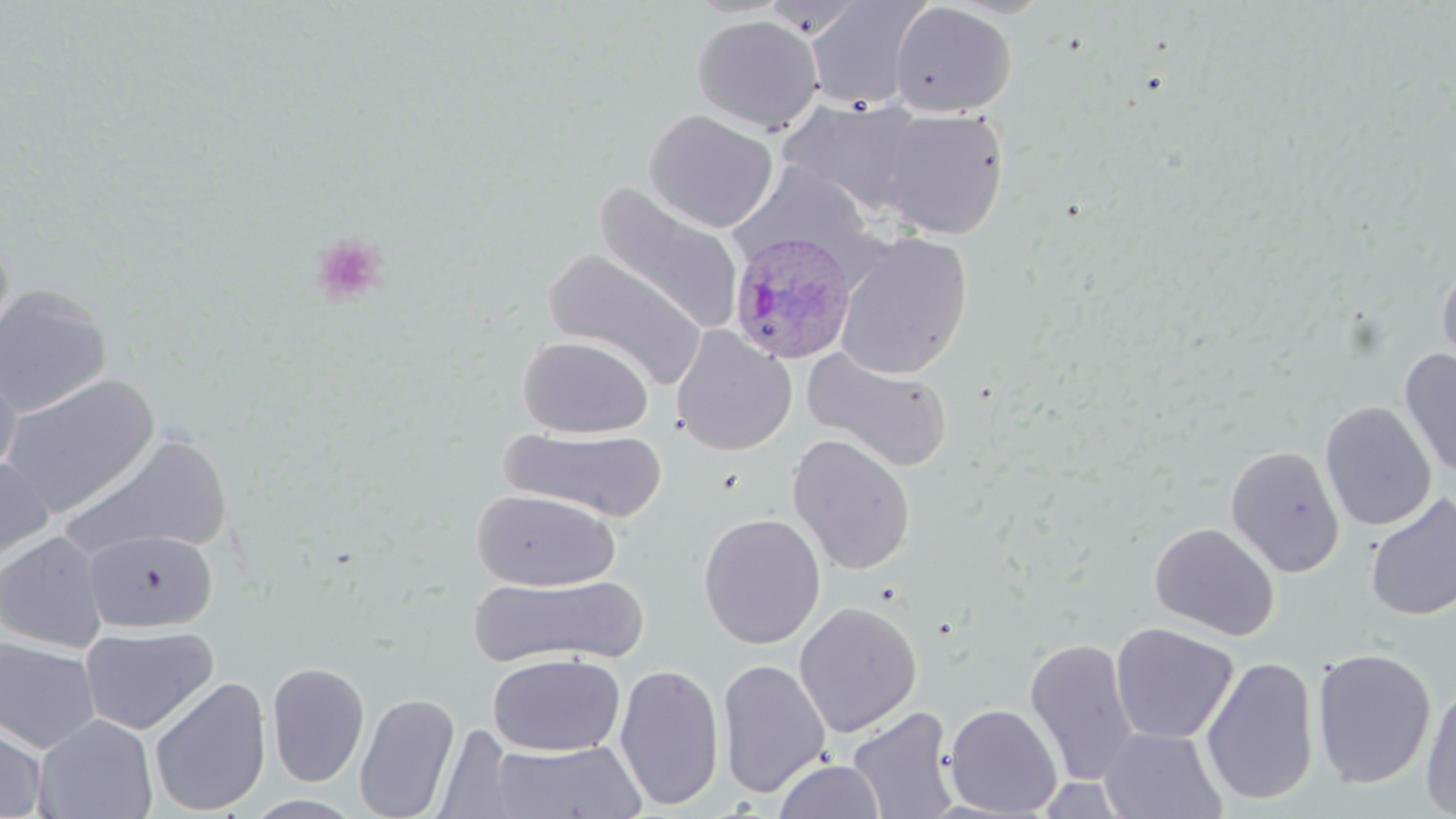

slide-level diagnosis = Plasmodium ovale
image size = 1456×819 pixels
stain = May-Grünwald-Giemsa
uninfected red blood cell locations = approximate bounding boxes as (x1, y1, x2, y2) in pixels: (803, 0, 931, 110), (888, 2, 1017, 118), (691, 14, 823, 134), (777, 96, 929, 217), (643, 109, 778, 232), (875, 109, 1010, 240), (726, 163, 878, 274), (593, 184, 744, 336), (834, 231, 973, 381), (543, 249, 709, 391), (1435, 260, 1456, 385), (0, 285, 113, 418), (671, 327, 797, 456), (517, 335, 653, 438), (802, 346, 954, 473), (1399, 348, 1456, 480), (0, 367, 21, 482), (0, 374, 160, 518), (1319, 400, 1436, 531), (502, 427, 669, 522), (58, 432, 233, 562), (787, 434, 917, 576), (1225, 445, 1345, 577), (0, 457, 54, 573), (471, 489, 620, 591), (1364, 493, 1456, 621), (698, 512, 826, 649), (1148, 522, 1280, 641), (82, 530, 219, 633), (0, 531, 109, 652), (469, 575, 648, 668), (794, 602, 923, 738), (1109, 622, 1239, 744), (80, 625, 219, 735), (0, 637, 101, 753), (1024, 637, 1139, 784), (1311, 647, 1436, 789), (487, 653, 625, 757), (1201, 656, 1320, 807), (716, 658, 832, 797), (266, 661, 370, 787), (613, 662, 725, 810), (149, 676, 272, 816), (1419, 683, 1456, 818), (354, 693, 461, 819), (943, 703, 1063, 817), (846, 706, 960, 819), (33, 713, 158, 819), (0, 724, 47, 818), (433, 724, 517, 819), (1100, 727, 1228, 819), (491, 739, 646, 818), (773, 758, 885, 819), (243, 794, 367, 818)
magnification = 1000x
modality = optical microscopy
Plasmodium ovale-infected red blood cell locations = approximate bounding boxes as (x1, y1, x2, y2) in pixels: (728, 231, 858, 363)
field of view = one of a larger specimen
preparation = thin blood smear
platelet locations = approximate bounding boxes as (x1, y1, x2, y2) in pixels: (310, 233, 389, 307)